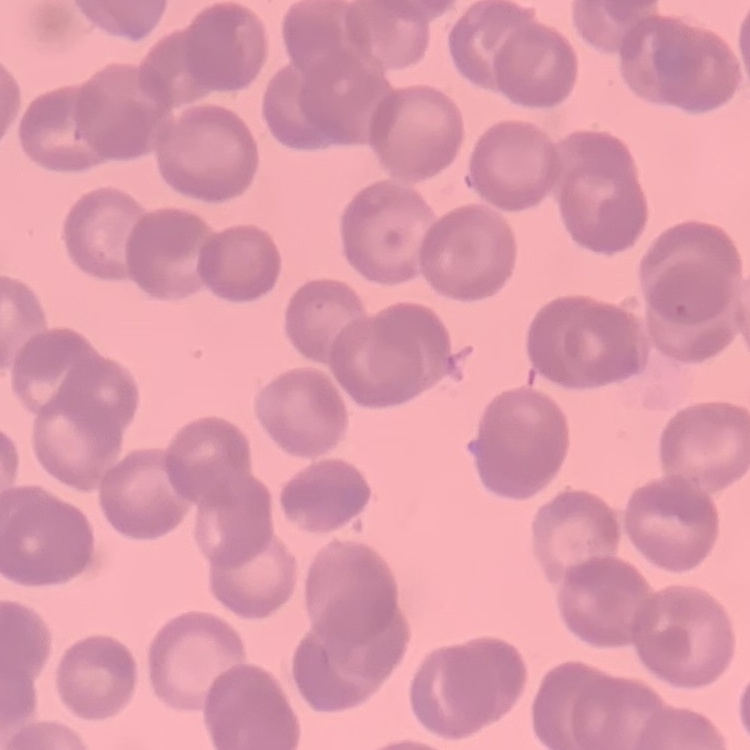
Summary:
  - Red blood cell morphology: rouleaux formation
  - Image type: square crop of a larger photomicrograph
  - Preparation: thin blood film
  - Stain: Field's or Giemsa